Describe the morphology of the erythrocytes.
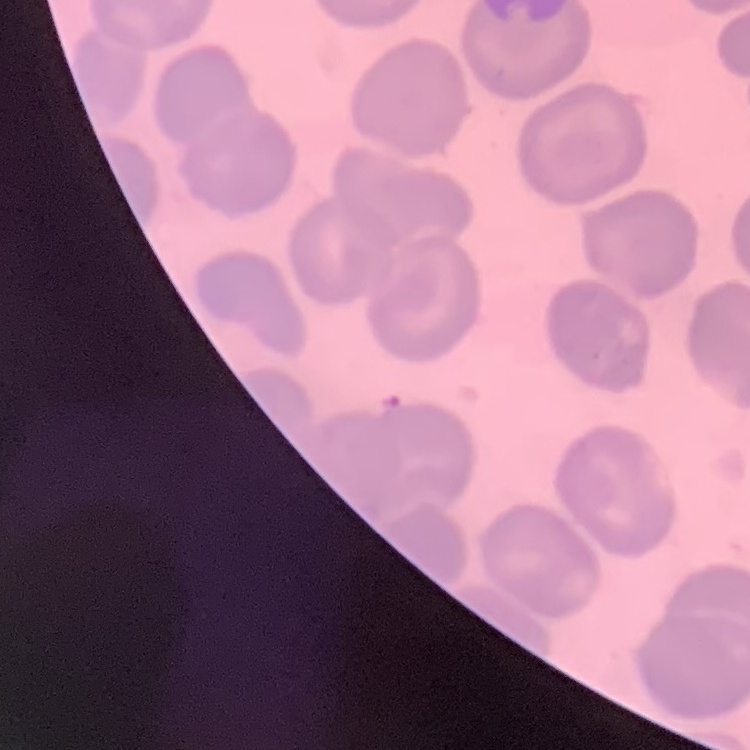

They show no rouleaux formation.

stain: Field's or Giemsa
preparation: thin blood film
image_type: one tile cut from a larger photomicrograph